State which parasite is depicted.
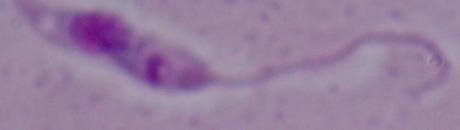

Leishmania.

Photomicrograph. 1000x magnification.